Point out each Plasmodium parasite.
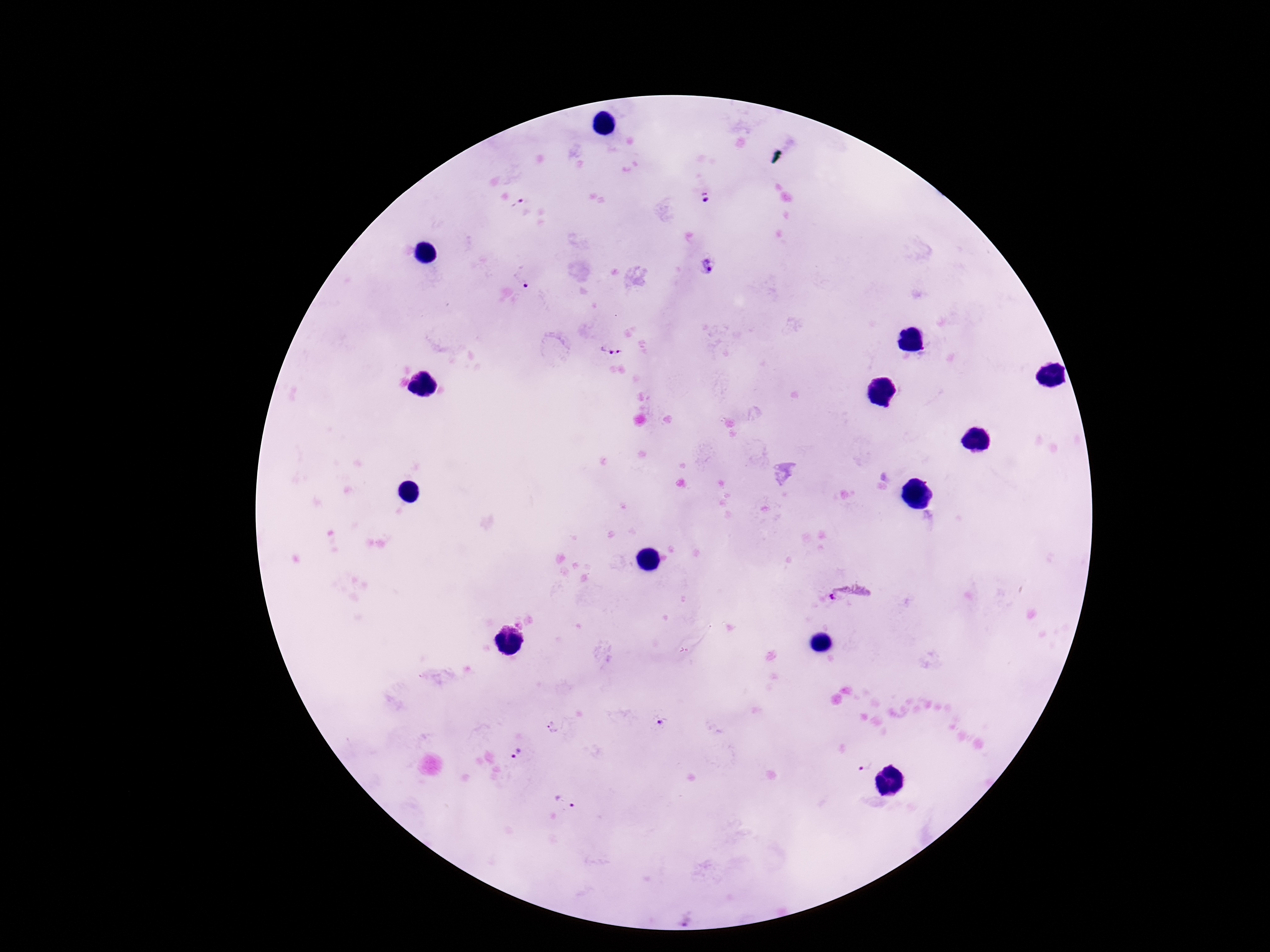

Approximate object centers, in pixels from the top-left corner.
Plasmodium parasites: (x=706, y=197), (x=518, y=203), (x=709, y=267), (x=525, y=284), (x=612, y=352), (x=847, y=593), (x=662, y=721), (x=554, y=727), (x=516, y=755), (x=865, y=766), (x=564, y=802).

Summary:
  - Magnification: 100x
  - Field of view: one from this slide
  - Capture: smartphone camera through the microscope eyepiece
  - Stain: Giemsa
  - Preparation: thick peripheral-blood smear
  - Image size: 1270×952 pixels
  - Patient malaria status: infected